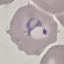 Malaria status: parasitized. Automatically extracted cell patch, resized to 64 × 64 pixels. Photographed with a smartphone camera at the microscope eyepiece. Giemsa stain. Thin blood film.